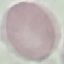

Malaria status: uninfected. Giemsa-stained preparation. Cell patch, automatically extracted from a larger field of view and resized to 64 × 64 pixels. Thin blood smear. Photographed with a smartphone camera at the microscope eyepiece.